Evaluate for malaria.
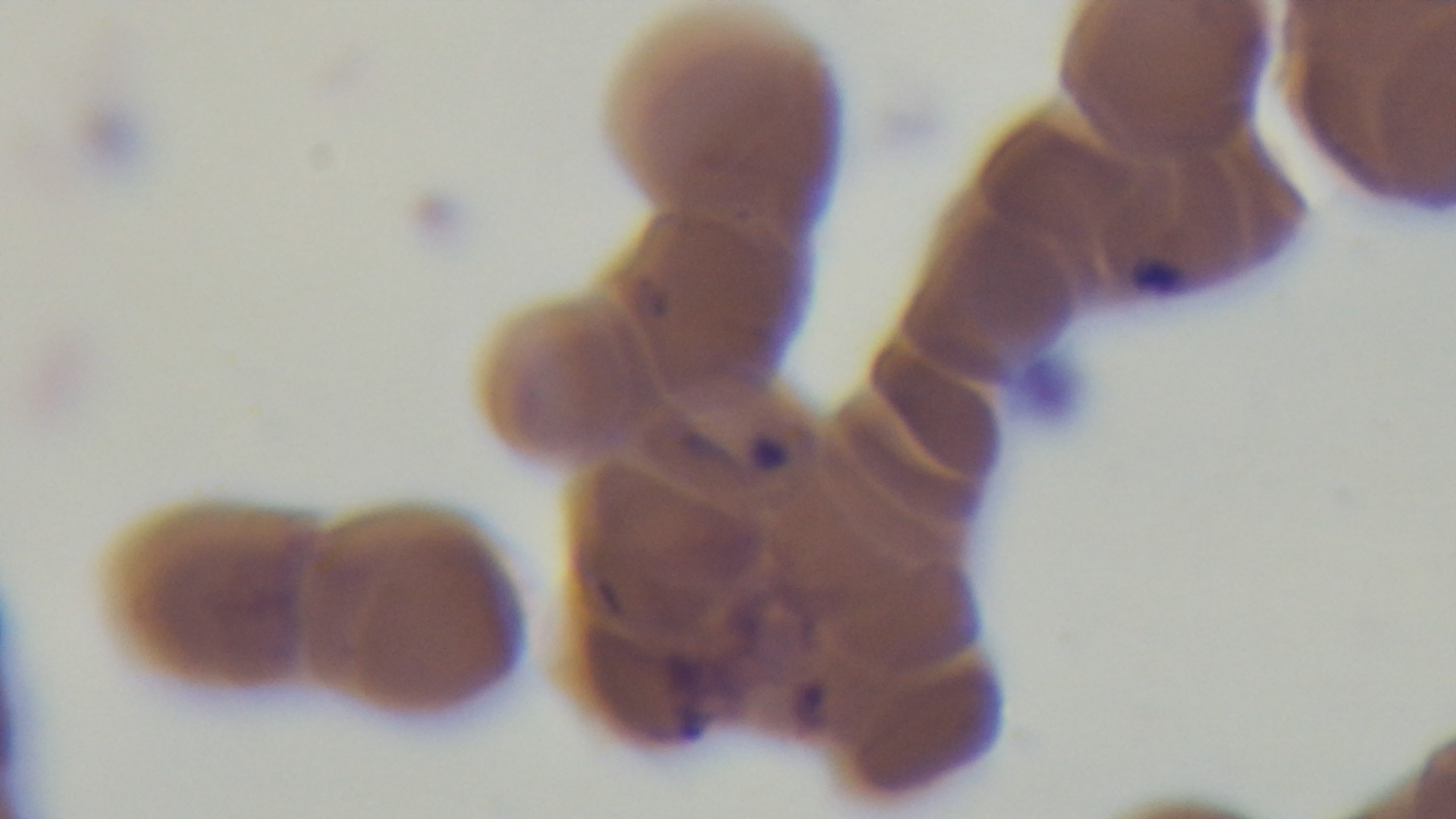
Infected.

100x oil-immersion objective. One field from the slide. Giemsa stain. Photomicrograph. Captured with a mounted 4K digital camera. Preparation: thin smear.